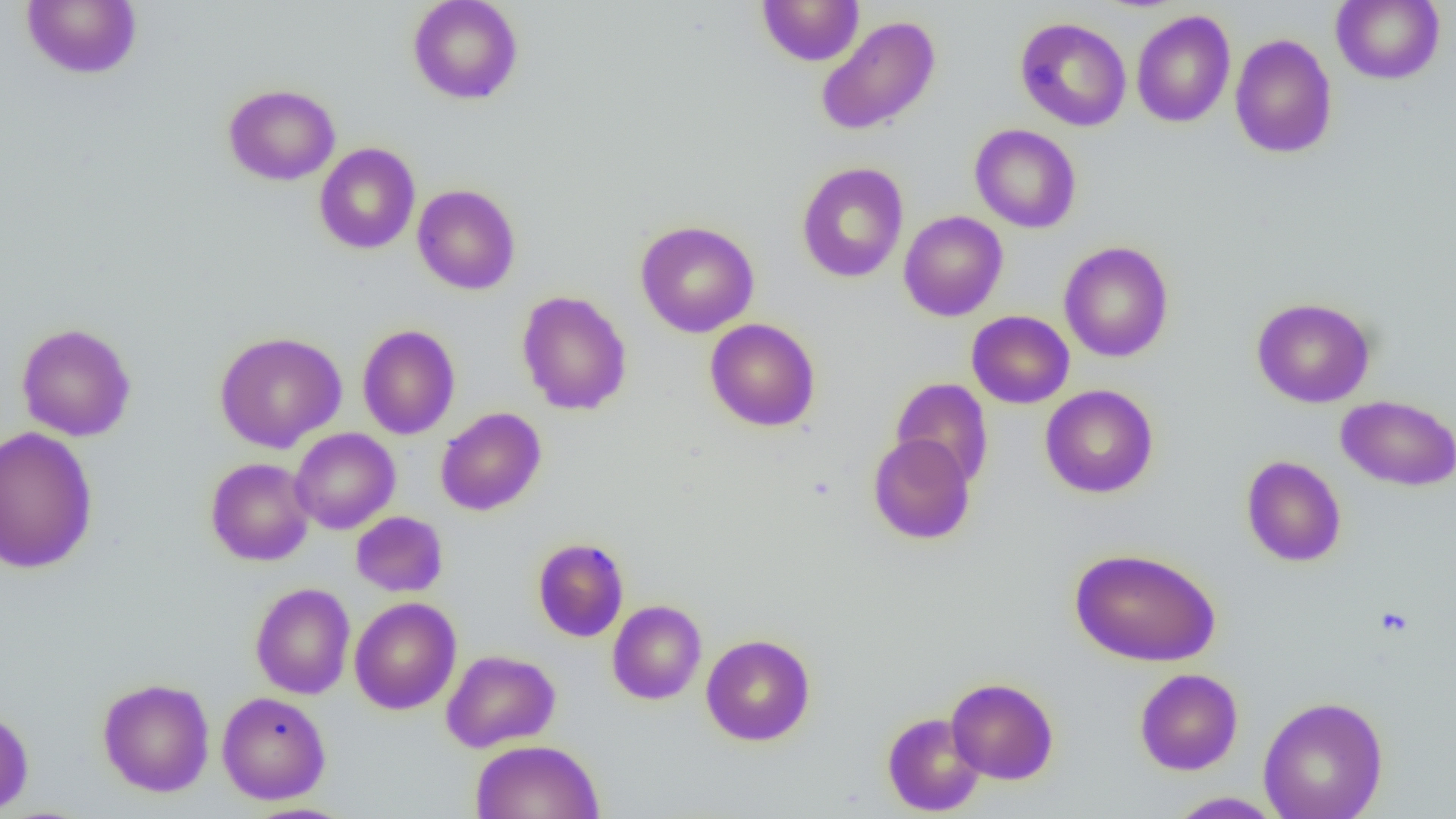
slide-level diagnosis = negative for blood parasites
modality = optical microscopy
uninfected red blood cell locations = approximate bounding boxes as (x1,y1)-(x2,y2) corner pairs in pixels: (21,0)-(142,79), (407,0)-(524,105), (756,0)-(865,66), (1331,0)-(1445,85), (1131,10)-(1235,128), (815,15)-(941,136), (1015,16)-(1132,132), (1229,33)-(1338,159), (223,83)-(340,185), (970,124)-(1082,233), (314,142)-(420,254), (796,161)-(909,283), (412,184)-(520,295), (898,211)-(1008,321), (635,220)-(760,338), (1058,241)-(1174,362), (516,290)-(632,416), (1251,297)-(1376,408), (967,310)-(1074,409), (704,318)-(820,432), (15,322)-(137,442), (357,324)-(460,440), (214,331)-(347,453), (890,378)-(994,488), (1041,384)-(1158,499), (1336,395)-(1456,491), (435,407)-(546,516), (0,425)-(99,575), (290,428)-(400,534), (867,433)-(976,544), (1241,456)-(1346,567), (205,457)-(315,566), (351,511)-(447,597), (532,538)-(629,642), (1069,547)-(1222,666), (250,582)-(355,699), (349,596)-(462,715), (607,600)-(706,704), (701,634)-(816,746), (441,649)-(560,753), (1134,668)-(1243,775), (946,677)-(1059,785), (97,678)-(215,797), (217,691)-(331,804), (1258,695)-(1388,819), (0,708)-(34,815), (881,711)-(985,816), (470,739)-(604,819), (1166,791)-(1285,818)
magnification = 1000x
image size = 1456×819 pixels
preparation = thin blood film
field of view = single